Evaluate for malaria.
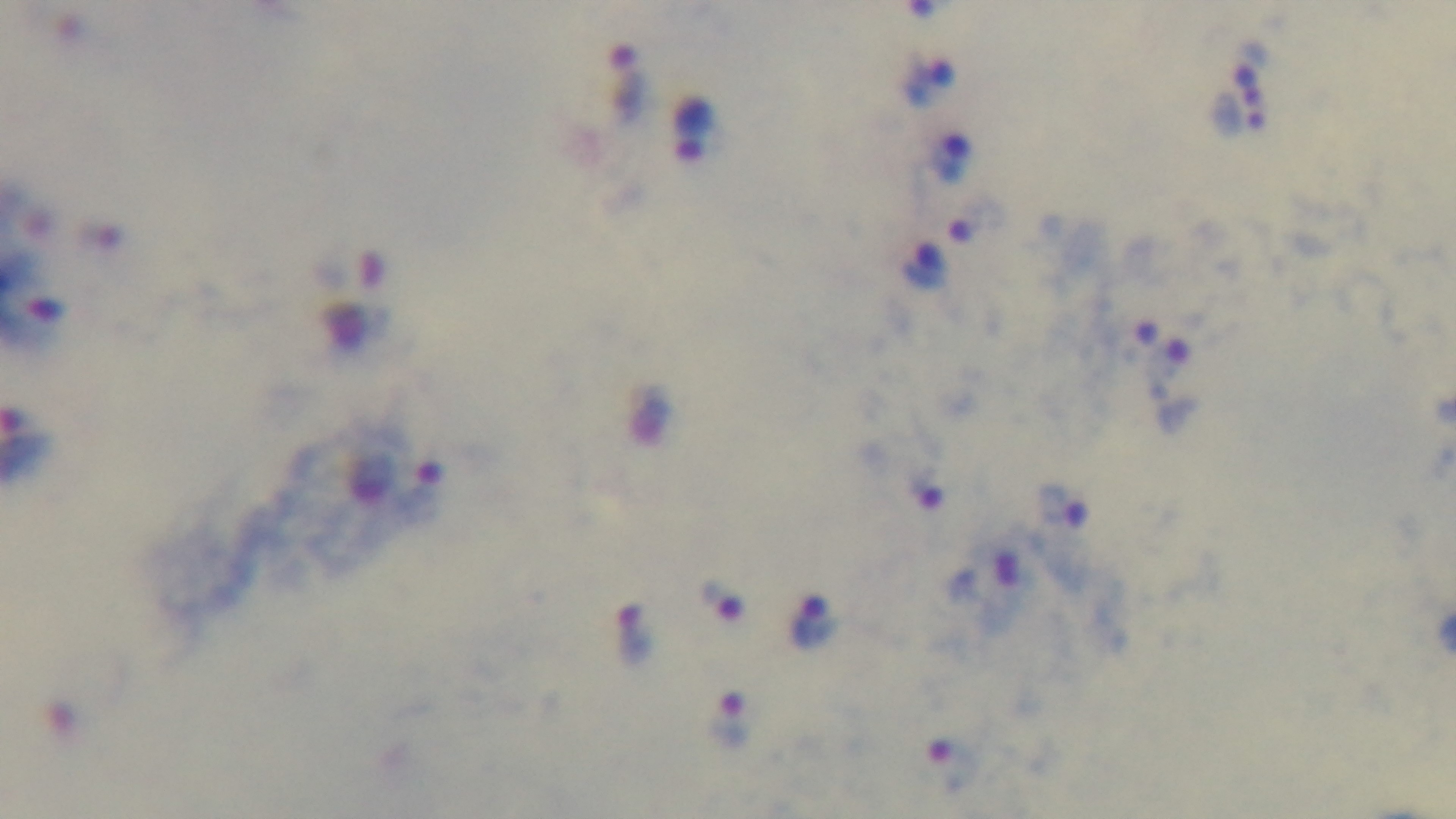

It is infected.

Preparation: thick smear. Single field of view. 100x oil-immersion objective. Photomicrograph. Giemsa-stained. Mounted 4K digital camera.